Comment on the morphology of the red blood cells.
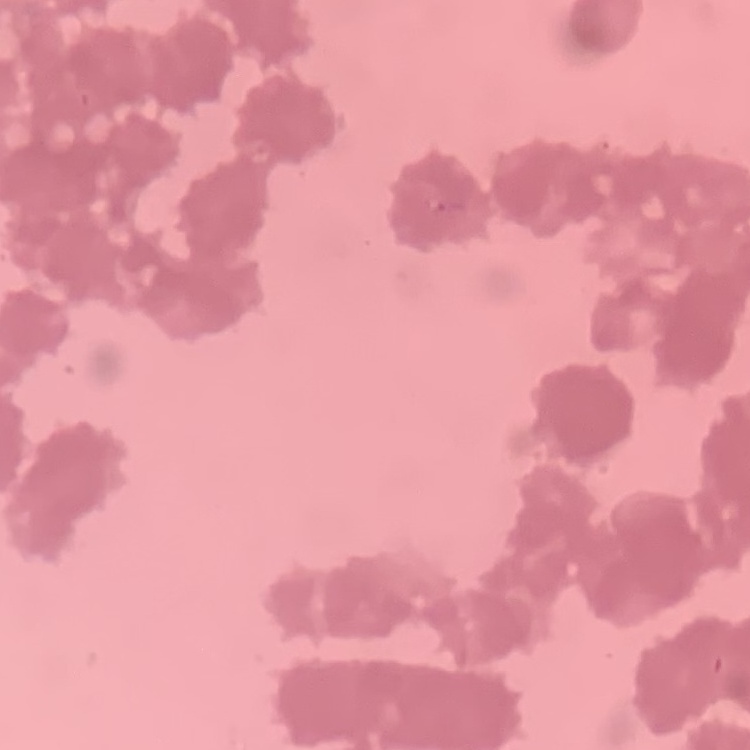
They show rouleaux formation.

preparation = thin blood film
stain = Field's or Giemsa
image type = square crop of a larger photomicrograph